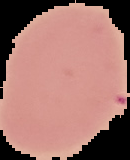

Malaria status: uninfected. Cell region segmented out of the field of view; the surrounding area is masked to black. From a thin blood smear. Image is 130×160 pixels.